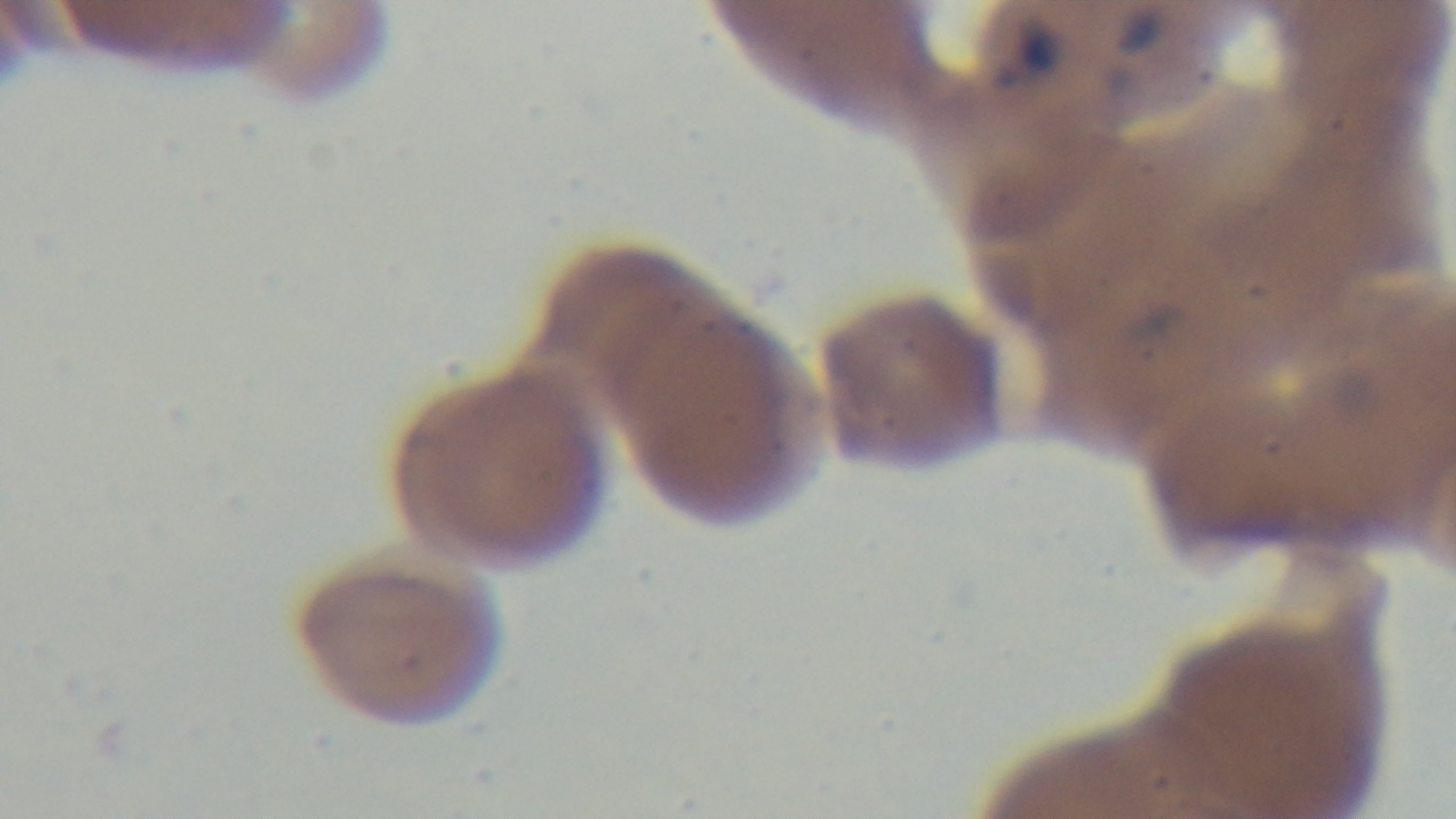
Single field of view. 100x oil-immersion objective. Mounted 4K digital camera. Malaria status: positive. Giemsa stain. Photomicrograph. Preparation: thin blood film.